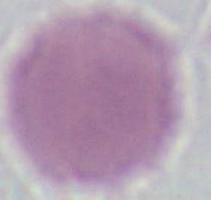

Summary:
  - Magnification: 1000x
  - Modality: micrograph
  - Identification: erythrocyte